Classify this cell by malaria status.
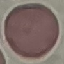

It is uninfected.

Summary:
  - Image type: automatically extracted cell patch, resized to 64 × 64 pixels
  - Preparation: thin blood film
  - Stain: Giemsa
  - Capture: smartphone through the microscope eyepiece